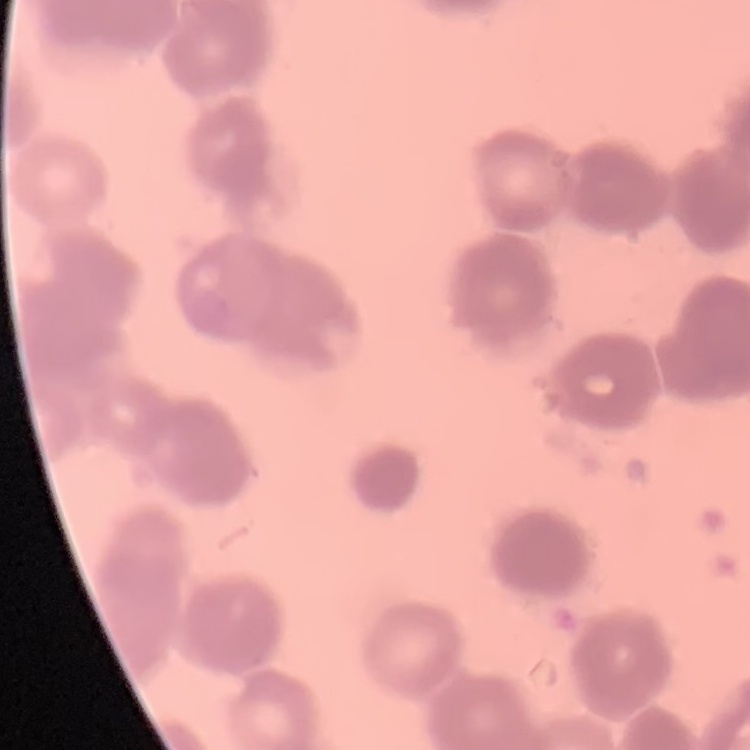

{
  "erythrocyte_morphology": "rouleaux formation",
  "stain": "Field's or Giemsa",
  "image_type": "square crop of a larger photomicrograph",
  "preparation": "thin blood film"
}